Report the malaria status of this cell.
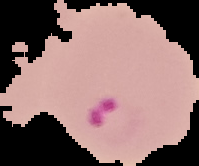

It is parasitized.

Summary:
  - Preparation: thin blood film
  - Image size: 199×166 pixels
  - Image type: segmented cell region on a black background